Report the malaria status of this cell.
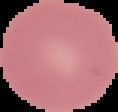

It is uninfected.

Image is 118×112 pixels. From a thin blood smear. The area outside the segmented cell region is set to black.